Assess this cell for malaria.
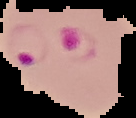
Parasitized.

image_size: 136×118 pixels
preparation: thin blood smear
image_type: segmented cell region with the area outside set to black